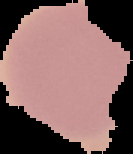
Cell region segmented out of the field of view; the surrounding area is masked to black. From a thin blood film. Malaria status: uninfected. Image is 133×154 pixels.